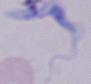

Summary:
  - Magnification: 1000x
  - Identification: trypanosome
  - Modality: micrograph